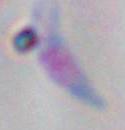
identification: Toxoplasma gondii
modality: micrograph
magnification: 1000x